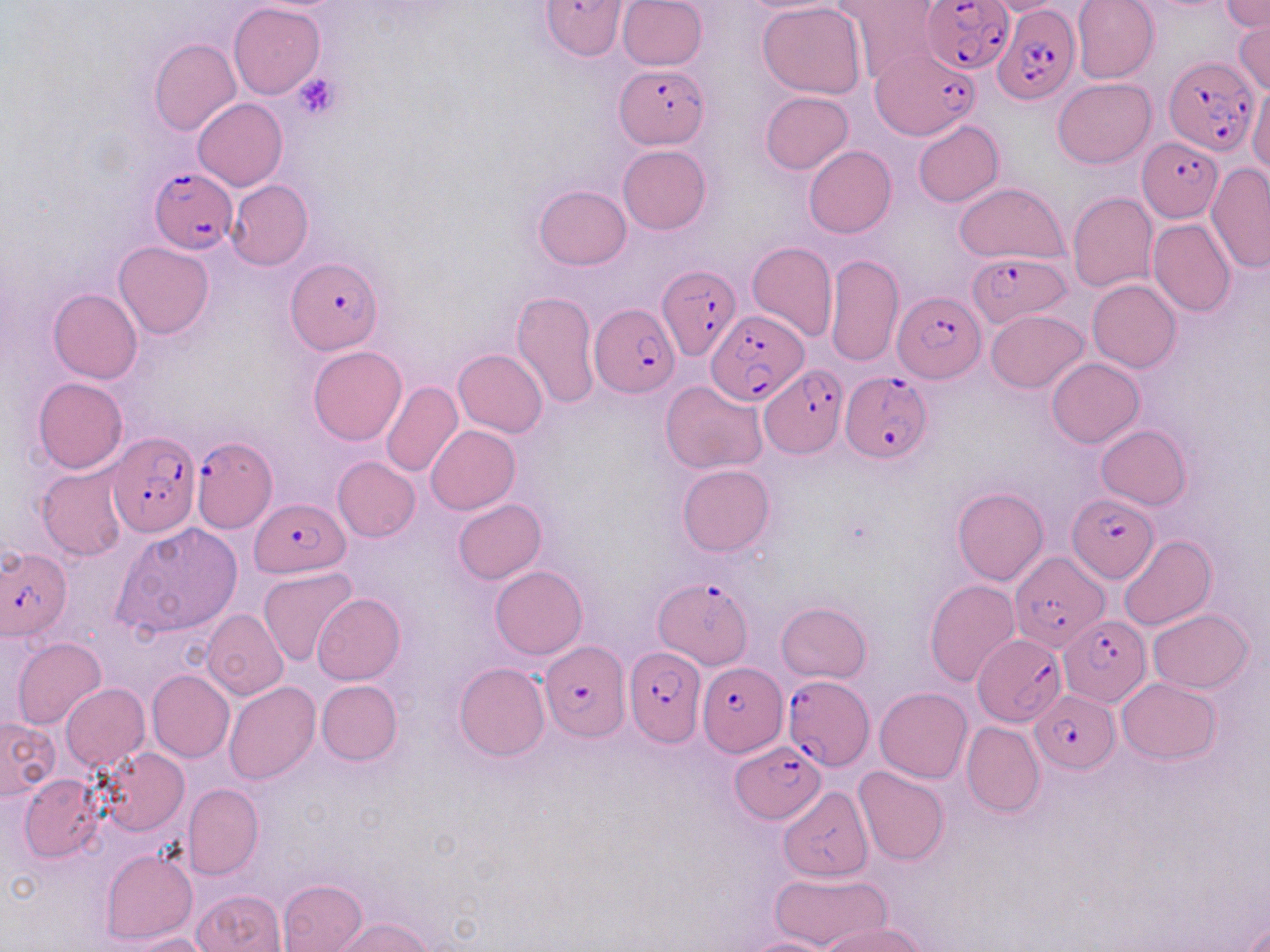 Approximate bounding boxes as (x1,y1)-(x2,y2) corner pairs in pixels. Plasmodium falciparum-infected red blood cell locations: (540,0)-(625,60), (922,0)-(1014,73), (993,6)-(1079,104), (869,46)-(979,139), (1165,55)-(1260,156), (614,63)-(711,148), (1140,138)-(1222,221), (148,165)-(237,254), (967,250)-(1071,326), (287,258)-(381,353), (656,264)-(740,360), (893,290)-(983,383), (589,304)-(681,398), (706,309)-(809,404), (760,365)-(846,458), (842,374)-(932,463), (108,432)-(199,537), (193,437)-(276,531), (1067,493)-(1159,583), (253,499)-(348,578), (0,547)-(71,639), (1012,550)-(1108,652), (655,576)-(753,668), (1059,615)-(1150,705), (972,629)-(1066,729), (540,638)-(627,740), (624,646)-(706,746), (697,660)-(785,755), (782,674)-(873,770), (1032,688)-(1119,772), (728,739)-(826,823). Uninfected red blood cell locations: (617,0)-(707,69), (1072,0)-(1159,83), (1222,0)-(1269,32), (839,1)-(942,83), (979,1)-(1072,16), (758,2)-(866,99), (229,3)-(325,99), (1234,17)-(1270,94), (149,38)-(240,137), (1053,78)-(1155,167), (1249,83)-(1270,176), (760,91)-(852,173), (194,97)-(287,191), (913,120)-(1003,207), (618,144)-(711,233), (804,146)-(896,238), (1206,162)-(1270,274), (226,179)-(314,270), (954,183)-(1066,262), (535,184)-(630,269), (1068,192)-(1158,292), (1095,215)-(1198,307), (1147,218)-(1236,317), (747,241)-(837,342), (115,242)-(213,339), (827,253)-(902,367), (1087,279)-(1181,373), (49,288)-(142,384), (511,290)-(598,409), (986,310)-(1089,393), (308,345)-(407,445), (454,348)-(547,437), (1046,358)-(1144,448), (34,377)-(128,472), (381,381)-(462,479), (661,381)-(768,474), (426,425)-(519,514), (1096,426)-(1191,510), (333,457)-(420,542), (678,465)-(774,557), (37,467)-(129,560), (952,488)-(1049,585), (454,499)-(546,583), (113,521)-(244,640), (1118,535)-(1216,630), (490,566)-(586,659), (259,568)-(359,666), (925,579)-(1021,686), (312,593)-(405,685), (776,602)-(870,683), (1147,609)-(1254,693), (202,610)-(288,700), (13,637)-(105,731), (454,662)-(550,761), (147,670)-(234,762), (1115,677)-(1221,764), (317,680)-(402,765), (224,681)-(320,784), (60,683)-(149,771), (875,687)-(972,783), (0,717)-(58,798), (961,721)-(1045,816), (99,748)-(189,835), (853,767)-(948,866), (20,773)-(105,862), (183,783)-(263,879), (777,786)-(874,915), (102,847)-(197,945), (769,870)-(889,948), (278,878)-(368,951), (193,890)-(286,952), (330,917)-(432,952), (820,921)-(931,952), (122,933)-(217,952), (735,935)-(841,952). Platelet locations: (291,71)-(343,119). Slide-level diagnosis: Plasmodium falciparum. Optical microscopy. One field of a larger specimen. Captured at 1000x magnification. Image is 1270×952 pixels. May-Grünwald-Giemsa-stained preparation. Thin blood smear.